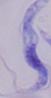
Photomicrograph. A trypanosome is shown. Captured at 1000x magnification.